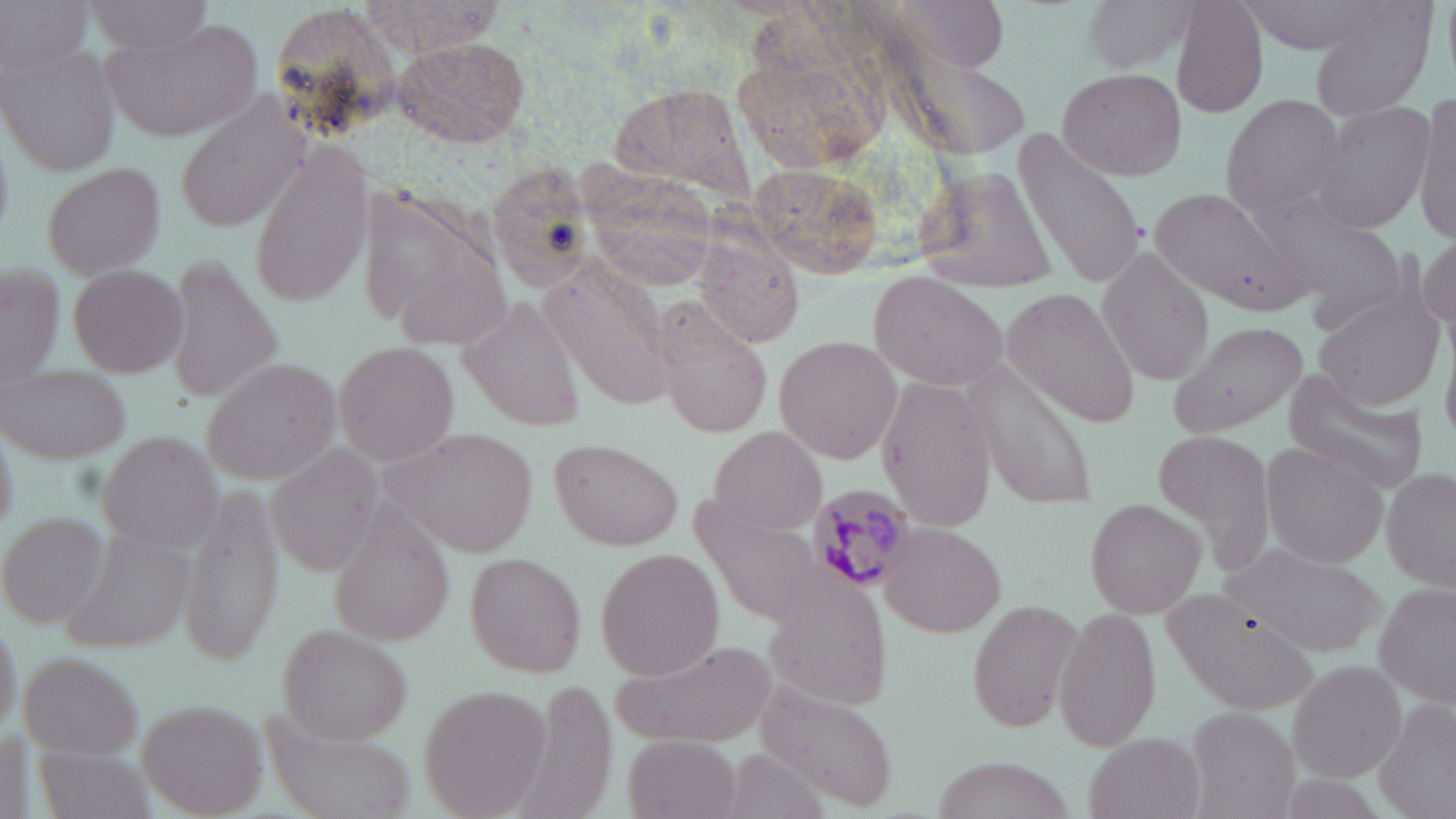
Approximate bounding boxes as [x1, y1, x2, y2] in pixels. Plasmodium malariae-infected red blood cell locations: [804, 484, 918, 597]. Uninfected red blood cell locations: [0, 0, 96, 87], [888, 0, 1009, 74], [1079, 0, 1205, 77], [1168, 0, 1270, 117], [1235, 0, 1401, 56], [1310, 1, 1438, 121], [82, 2, 219, 55], [102, 16, 266, 145], [395, 34, 530, 150], [1, 36, 120, 175], [1056, 66, 1188, 182], [609, 80, 753, 198], [1218, 92, 1348, 216], [1414, 92, 1456, 241], [173, 96, 309, 234], [1307, 101, 1434, 233], [1013, 132, 1147, 290], [248, 142, 376, 308], [746, 159, 888, 277], [42, 161, 166, 281], [914, 164, 1060, 297], [1147, 186, 1313, 321], [1252, 187, 1404, 313], [1415, 229, 1455, 339], [1096, 247, 1215, 386], [163, 257, 286, 406], [540, 258, 681, 409], [67, 262, 189, 378], [3, 263, 62, 386], [867, 268, 1014, 393], [1002, 286, 1141, 430], [459, 296, 586, 433], [1313, 296, 1445, 409], [656, 307, 773, 442], [1168, 318, 1309, 436], [774, 334, 903, 465], [333, 341, 459, 465], [200, 357, 343, 484], [964, 362, 1100, 512], [2, 364, 128, 464], [1279, 369, 1427, 493], [877, 379, 999, 530], [1149, 425, 1279, 571], [386, 426, 538, 558], [711, 426, 826, 536], [99, 431, 223, 551], [548, 436, 684, 550], [1257, 441, 1388, 568], [266, 444, 387, 575], [1379, 466, 1456, 593], [183, 479, 286, 665], [1086, 497, 1206, 618], [327, 500, 455, 649], [696, 505, 827, 624], [1, 509, 112, 627], [879, 522, 1003, 638], [63, 527, 198, 658], [1223, 540, 1384, 657], [596, 548, 725, 682], [464, 550, 588, 679], [761, 574, 895, 712], [1373, 578, 1455, 707], [1163, 592, 1320, 715], [965, 596, 1084, 734], [0, 605, 21, 747], [1054, 605, 1163, 754], [278, 624, 413, 745], [608, 638, 779, 750], [18, 650, 145, 758], [1285, 659, 1407, 784], [751, 679, 900, 814], [510, 681, 615, 819], [417, 682, 552, 819], [1373, 694, 1456, 819], [138, 700, 265, 815], [1181, 704, 1302, 819], [261, 709, 418, 819], [1080, 731, 1206, 819], [623, 734, 741, 819], [36, 744, 152, 819]. Slide-level diagnosis: Plasmodium malariae. 1000x magnification. Thin blood film. Image is 1456×819 pixels. Optical microscopy. May-Grünwald-Giemsa-stained preparation. Single field of view.